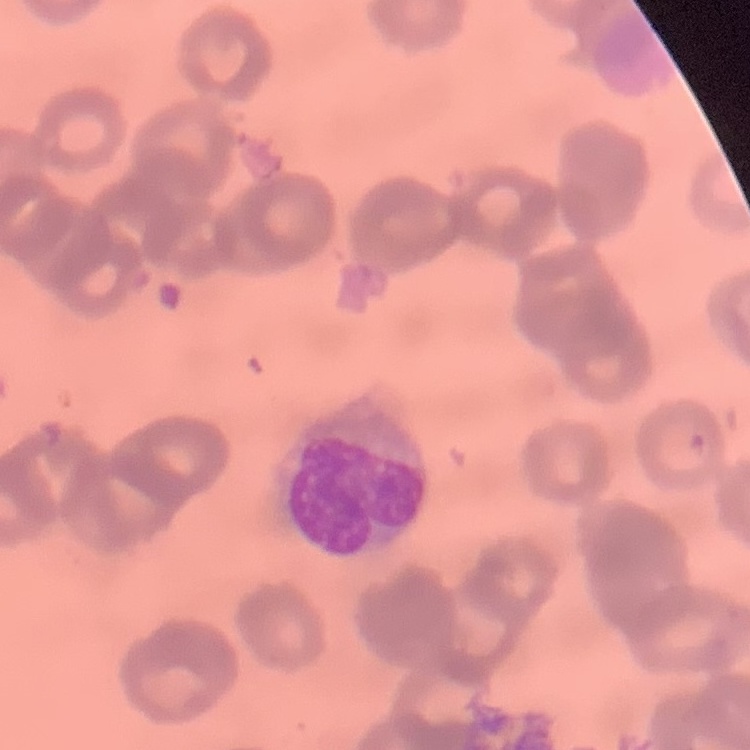
The red blood cells show rouleaux formation. One tile cut from a larger photomicrograph. Thin blood film. Field's or Giemsa stain.